Describe the morphology of the erythrocytes.
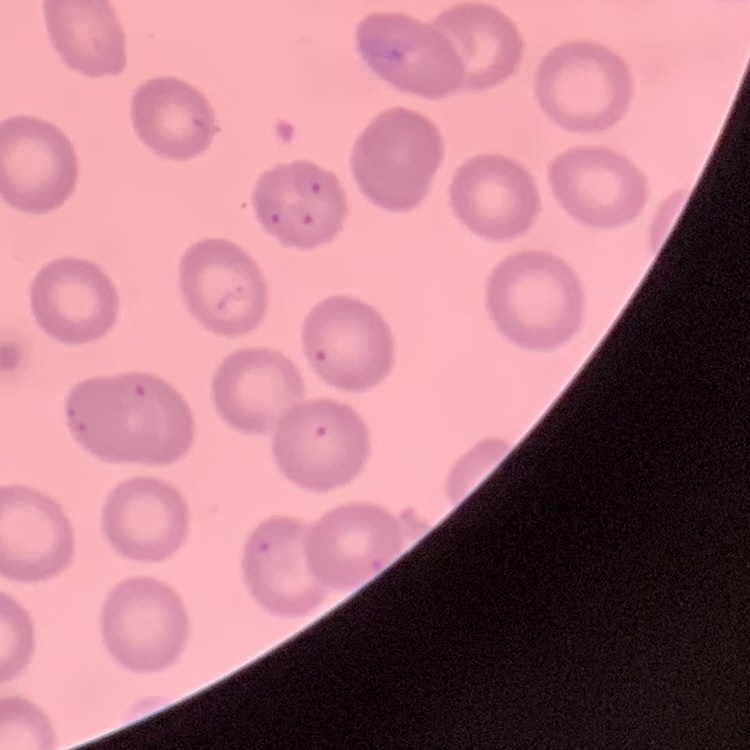
No rouleaux formation.

Summary:
  - Stain: Field's or Giemsa
  - Preparation: thin blood smear
  - Image type: one tile cut from a larger photomicrograph